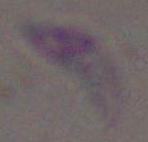
modality = micrograph
magnification = 1000x
identification = Toxoplasma gondii